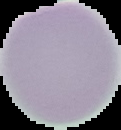

Image is 121×130 pixels. Segmented cell region on a black background. From a thin blood film. Result: negative for malaria parasites.